Describe the morphology of the red blood cells.
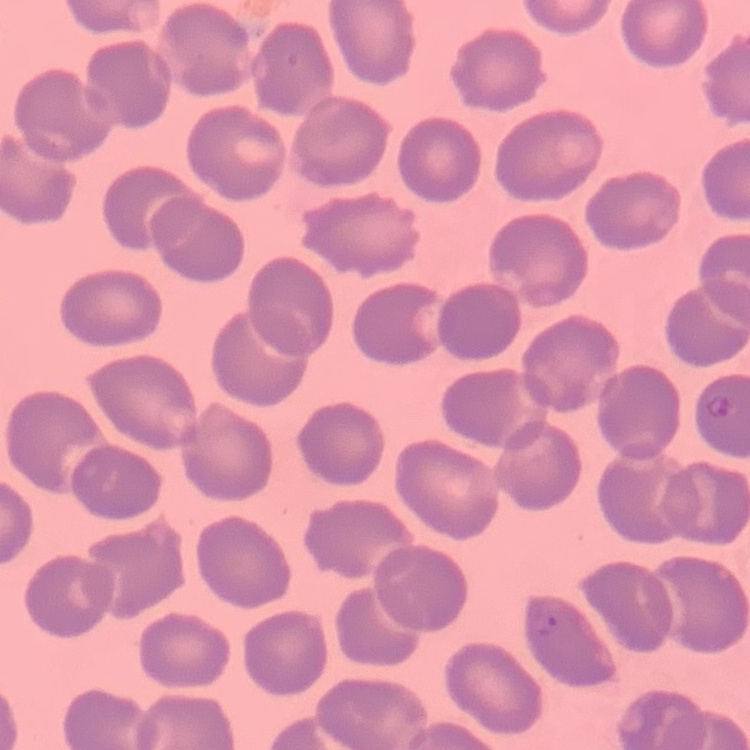

No rouleaux formation.

image_type: square crop of a larger photomicrograph
stain: Field's or Giemsa
preparation: thin blood smear